Report the malaria status.
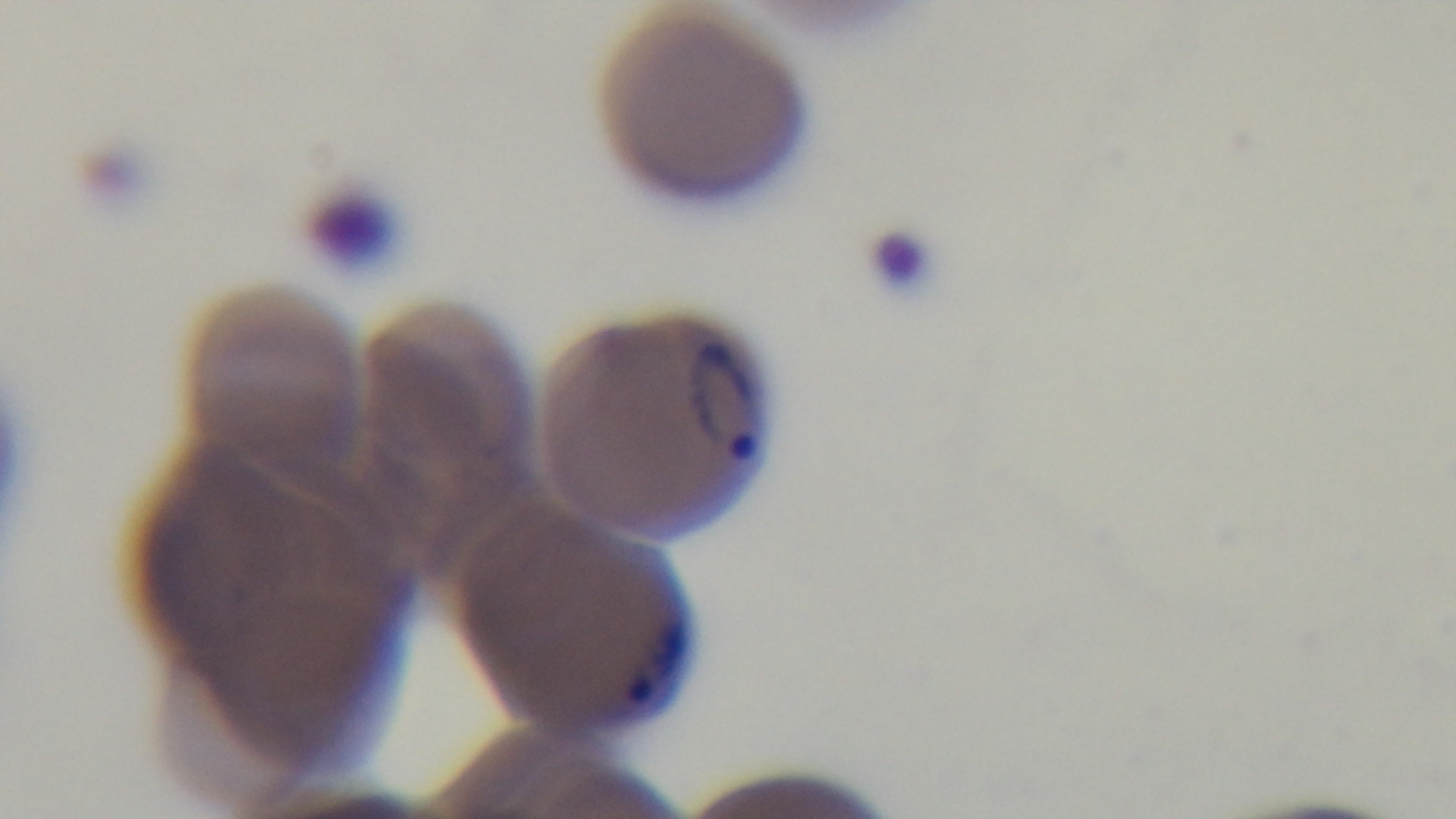
It is infected.

Light microscopy. 100x oil-immersion objective. Giemsa-stained. Preparation: thin. Mounted 4K digital camera. One field from the slide.